Report the malaria status of this cell.
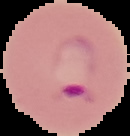

It is parasitized.

image size = 130×136 pixels
preparation = thin blood film
image type = cell region segmented out of the field of view; surrounding area masked to black